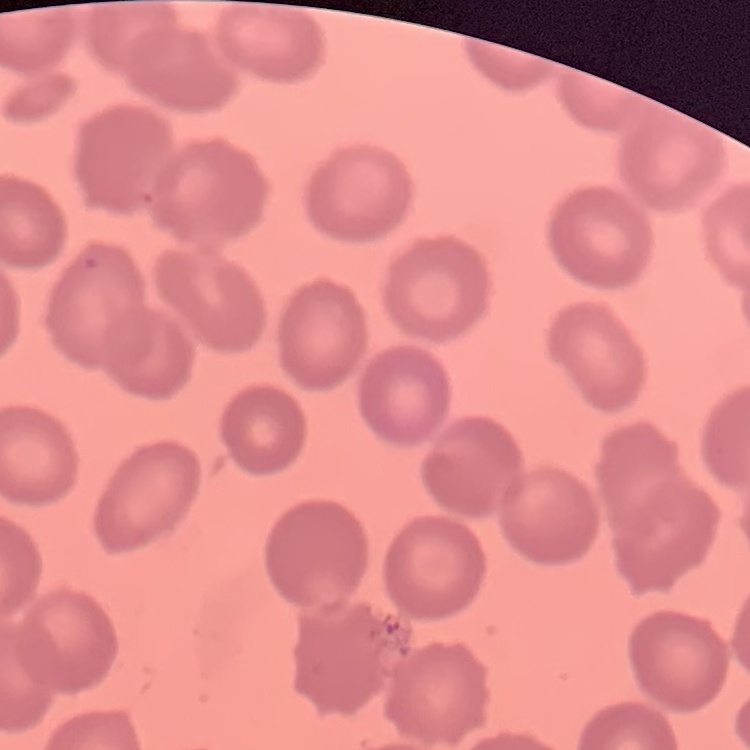

The red blood cells exhibit no rouleaux formation. Thin blood film. Square crop of a larger photomicrograph. Field's or Giemsa stain.